Find each parasitized RBC.
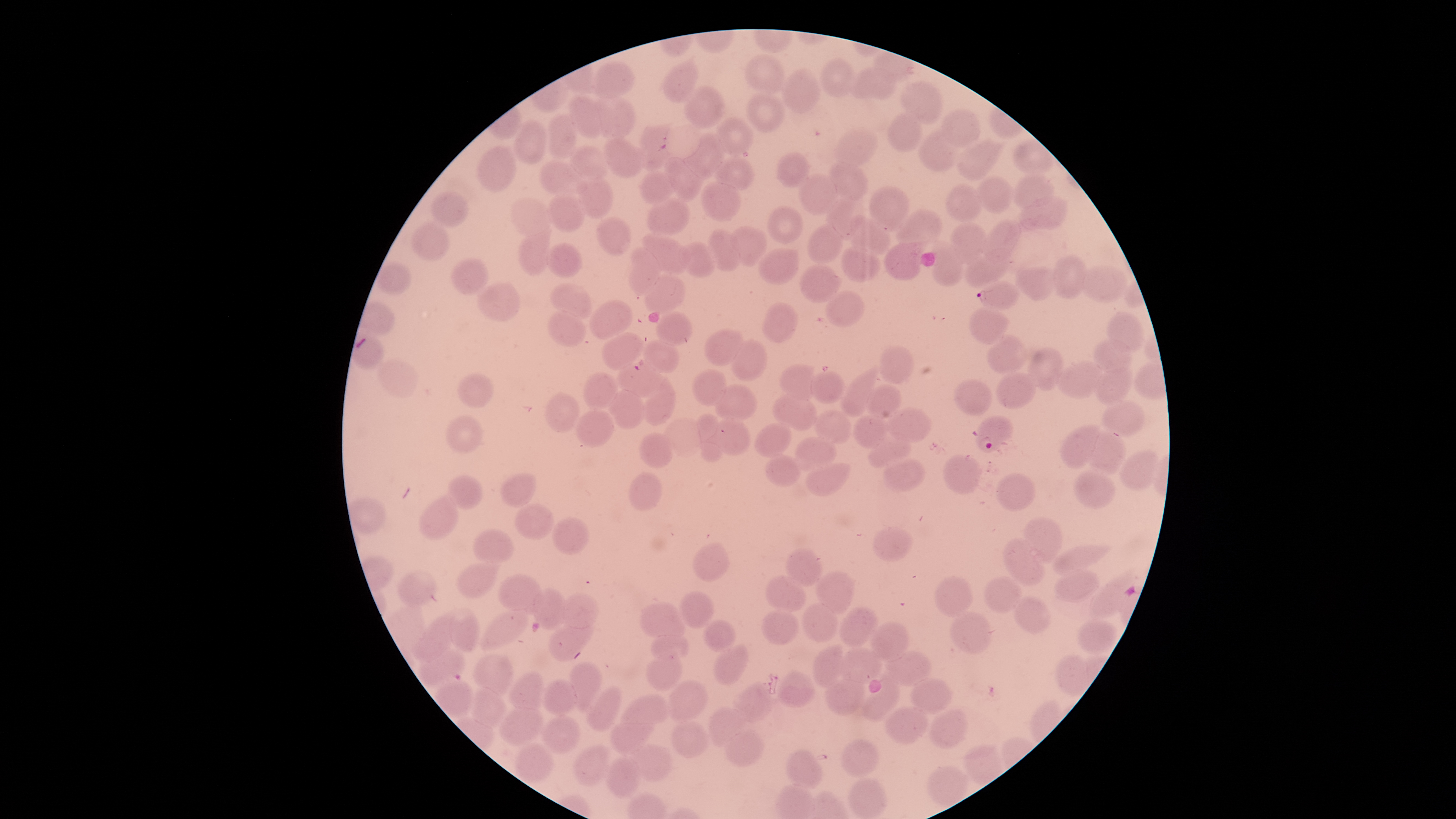
Approximate bounding boxes as (left, top, right, bottom) in pixels.
Parasitized RBCs: (977, 281, 1021, 311), (973, 415, 1013, 453), (418, 650, 465, 687).

Approximate bounding boxes as (left, top, right, bottom) in pixels. Uninfected RBCs: (745, 55, 784, 94), (820, 58, 854, 96), (595, 62, 635, 98), (664, 63, 700, 102), (850, 68, 897, 101), (782, 69, 820, 113), (902, 81, 942, 124), (683, 86, 724, 127), (747, 93, 784, 133), (566, 95, 604, 138), (596, 96, 635, 140), (942, 109, 981, 147), (546, 113, 578, 160), (886, 113, 922, 152), (716, 118, 754, 156), (514, 121, 546, 164), (638, 126, 673, 170), (835, 128, 878, 166), (917, 132, 958, 172), (685, 134, 725, 179), (603, 137, 647, 177), (958, 139, 1001, 180), (1014, 141, 1052, 177), (571, 145, 610, 179), (478, 146, 516, 192), (775, 152, 810, 186), (667, 157, 703, 203), (715, 157, 756, 191), (830, 160, 868, 199), (541, 161, 585, 198), (639, 171, 675, 206), (800, 174, 836, 214), (578, 175, 613, 218), (976, 175, 1011, 212), (1013, 176, 1053, 207), (701, 182, 741, 223), (946, 184, 981, 223), (869, 186, 910, 232), (432, 190, 467, 226), (548, 192, 584, 231), (1020, 196, 1067, 232), (647, 197, 690, 236), (827, 197, 864, 239), (511, 198, 551, 236), (768, 206, 803, 244), (897, 209, 941, 253), (596, 215, 631, 255), (848, 216, 890, 257), (412, 221, 449, 261), (982, 221, 1021, 261), (952, 223, 986, 264), (808, 225, 843, 264), (732, 227, 765, 265), (707, 229, 740, 271), (644, 232, 689, 275), (519, 233, 548, 274), (929, 240, 963, 286), (680, 242, 715, 277), (546, 243, 581, 277), (885, 244, 922, 282), (840, 246, 878, 282), (627, 247, 658, 296), (759, 248, 798, 284), (965, 249, 1009, 289), (1050, 255, 1087, 297), (452, 257, 487, 293), (377, 262, 411, 296), (1080, 264, 1128, 303), (799, 265, 840, 304), (1015, 266, 1054, 301), (645, 275, 686, 314), (477, 281, 519, 320), (553, 284, 591, 321), (826, 289, 866, 328), (590, 300, 633, 340), (762, 303, 797, 343), (971, 307, 1007, 342), (548, 310, 586, 344), (658, 311, 692, 347), (1108, 311, 1144, 352), (705, 329, 743, 366), (602, 331, 644, 368), (352, 335, 384, 370), (987, 335, 1026, 374), (645, 338, 679, 373), (1093, 338, 1132, 374), (732, 339, 767, 381), (878, 345, 915, 384), (1028, 347, 1064, 390), (380, 359, 416, 398), (618, 360, 660, 396), (1056, 361, 1101, 399), (779, 365, 815, 400), (1095, 367, 1134, 405), (691, 370, 727, 406), (840, 371, 878, 417), (996, 371, 1035, 409), (457, 372, 495, 408), (810, 372, 844, 404), (582, 373, 618, 409), (643, 379, 676, 425), (954, 379, 994, 416), (715, 384, 757, 419), (866, 385, 903, 419), (609, 390, 646, 426), (542, 392, 582, 432), (773, 394, 816, 430), (1102, 399, 1144, 437), (888, 407, 930, 442), (813, 409, 853, 444), (574, 410, 614, 447), (696, 413, 725, 461), (851, 414, 887, 449), (445, 415, 484, 452), (665, 418, 702, 457), (715, 418, 750, 456), (754, 422, 793, 458), (1061, 425, 1103, 467), (1089, 431, 1127, 474), (638, 432, 674, 469), (869, 433, 911, 466), (794, 436, 836, 471), (1119, 451, 1160, 489), (766, 455, 800, 486), (944, 455, 982, 495), (883, 456, 927, 493), (806, 462, 852, 497), (1073, 470, 1114, 508), (629, 471, 663, 512), (501, 473, 536, 507), (996, 473, 1036, 511), (447, 475, 482, 509), (350, 495, 387, 534), (418, 495, 457, 539), (514, 501, 554, 540), (551, 516, 590, 556), (1024, 516, 1063, 562), (872, 526, 913, 561), (473, 528, 514, 563), (1004, 538, 1044, 586), (693, 543, 731, 583), (1051, 544, 1107, 575), (786, 548, 824, 588), (457, 562, 498, 597), (1054, 569, 1100, 602), (398, 570, 436, 607), (1090, 570, 1134, 620), (817, 572, 854, 614), (500, 573, 542, 611), (766, 574, 806, 612), (935, 575, 974, 618), (984, 576, 1023, 615), (533, 588, 566, 629), (679, 591, 714, 629), (561, 593, 598, 628), (1012, 596, 1050, 635), (639, 601, 685, 637), (802, 602, 837, 642), (481, 607, 529, 649), (838, 607, 878, 648), (450, 609, 480, 652), (762, 610, 801, 645), (950, 612, 992, 654), (413, 613, 456, 662), (549, 617, 592, 660), (1077, 619, 1119, 655), (703, 620, 737, 653), (868, 622, 909, 662), (651, 630, 689, 660), (714, 644, 749, 685), (812, 645, 846, 685), (838, 648, 882, 683), (647, 651, 684, 691), (889, 651, 931, 686), (475, 654, 513, 695), (1055, 656, 1090, 696), (570, 663, 602, 709), (507, 670, 546, 710), (777, 672, 816, 709), (859, 677, 899, 722), (911, 677, 953, 715), (436, 678, 474, 716), (826, 678, 864, 716), (542, 679, 577, 716), (668, 681, 708, 720), (732, 682, 772, 723), (586, 686, 622, 731), (470, 687, 509, 727), (621, 695, 668, 726), (500, 706, 544, 746), (883, 706, 930, 745), (708, 707, 745, 748), (929, 709, 968, 749), (543, 715, 583, 753), (610, 715, 654, 754), (672, 720, 710, 757), (725, 730, 764, 766), (840, 739, 879, 778), (516, 742, 555, 783), (632, 744, 672, 782), (964, 744, 1003, 786), (574, 745, 612, 785), (785, 748, 823, 789), (606, 756, 641, 798), (927, 765, 967, 808), (848, 777, 887, 819). Photographed with a smartphone camera through the microscope eyepiece. Thin blood film. Giemsa-stained preparation. Species: Plasmodium falciparum. Image is 1456×819 pixels. Circular visible region. One field of view of the specimen.